Locate and identify every blood parasite.
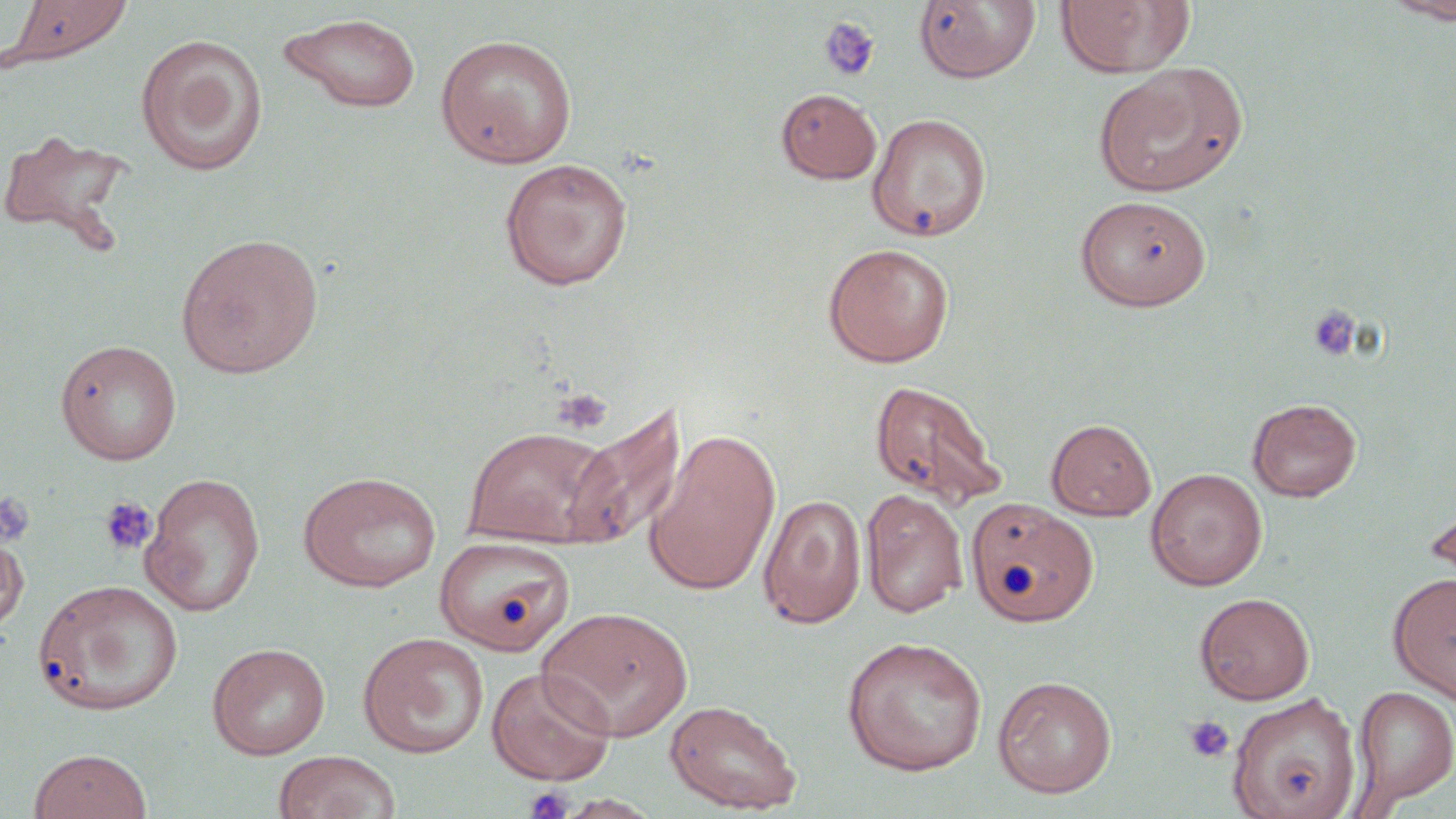
No blood parasites seen.

{
  "slide_level_diagnosis": "no evidence of blood parasites",
  "preparation": "thin blood film",
  "stain": "May-Grünwald-Giemsa",
  "magnification": "1000x",
  "platelet_locations": "approximate bounding boxes as (x1,y1)-(x2,y2) corner pairs in pixels: (818,15)-(880,82), (1307,305)-(1361,360), (552,387)-(612,434), (0,492)-(37,548), (99,496)-(157,557), (1183,715)-(1235,763), (523,786)-(574,819)",
  "field_of_view": "single",
  "uninfected_red_blood_cell_locations": "approximate bounding boxes as (x1,y1)-(x2,y2) corner pairs in pixels: (4,0)-(132,65), (914,0)-(1041,83), (1055,0)-(1194,78), (1382,0)-(1456,23), (279,13)-(422,113), (135,33)-(268,177), (436,34)-(577,167), (1095,64)-(1247,197), (777,88)-(882,183), (867,112)-(992,242), (0,128)-(135,256), (499,158)-(633,290), (1074,195)-(1211,311), (176,232)-(325,378), (822,242)-(955,367), (55,339)-(182,465), (869,379)-(1006,509), (1247,397)-(1361,501), (563,403)-(686,549), (1046,418)-(1156,520), (461,425)-(621,548), (643,430)-(781,596), (1146,468)-(1268,591), (297,470)-(441,592), (140,472)-(266,616), (860,489)-(969,618), (1421,490)-(1456,597), (758,493)-(866,628), (966,499)-(1100,628), (0,528)-(28,635), (434,535)-(575,655), (1387,570)-(1456,704), (33,578)-(184,715), (1194,592)-(1315,705), (536,606)-(693,742), (357,632)-(489,759), (841,636)-(988,775), (207,643)-(331,759), (486,665)-(616,786), (992,675)-(1117,799), (1352,686)-(1456,808), (1229,693)-(1361,819), (664,698)-(802,814), (29,748)-(152,819), (273,750)-(401,819), (557,794)-(662,818)",
  "modality": "optical microscopy",
  "image_size": "1456×819 pixels"
}